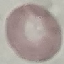
Summary:
  - Malaria status: uninfected
  - Stain: Giemsa
  - Capture: smartphone camera at the microscope eyepiece
  - Image type: cell patch, automatically extracted from a larger field of view and resized to 64 × 64 pixels
  - Preparation: thin blood smear